Identify the preparation type.
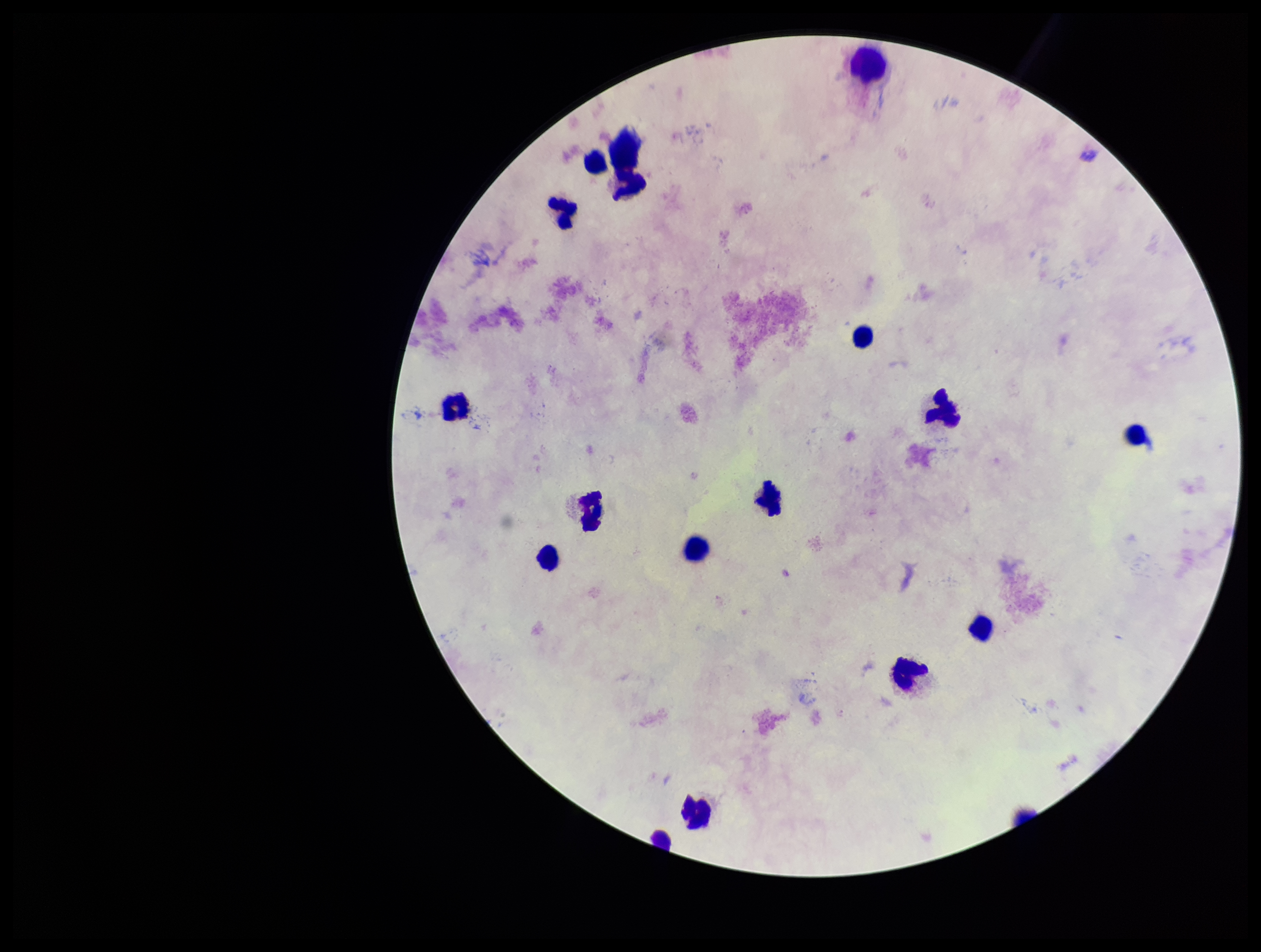
It is a thick blood smear.

field_of_view: one from this slide
plasmodium_parasites: none seen
parasite_count: 0
patient_malaria_status: negative
stain: Giemsa
capture: smartphone photograph through the microscope eyepiece
leukocyte_count: 16
image_size: 1261×952 pixels